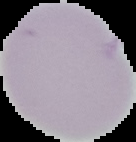
preparation = thin blood smear
image size = 136×142 pixels
result = negative for malaria parasites
image type = segmented cell region with the area outside set to black